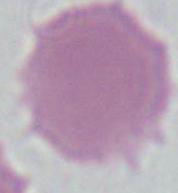
A red blood cell is shown. Photomicrograph. 1000x magnification.